Report the malaria status of this cell.
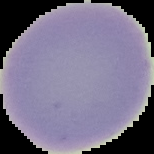

Uninfected.

Summary:
  - Image size: 154×154 pixels
  - Preparation: thin blood smear
  - Image type: segmented cell region with the area outside set to black